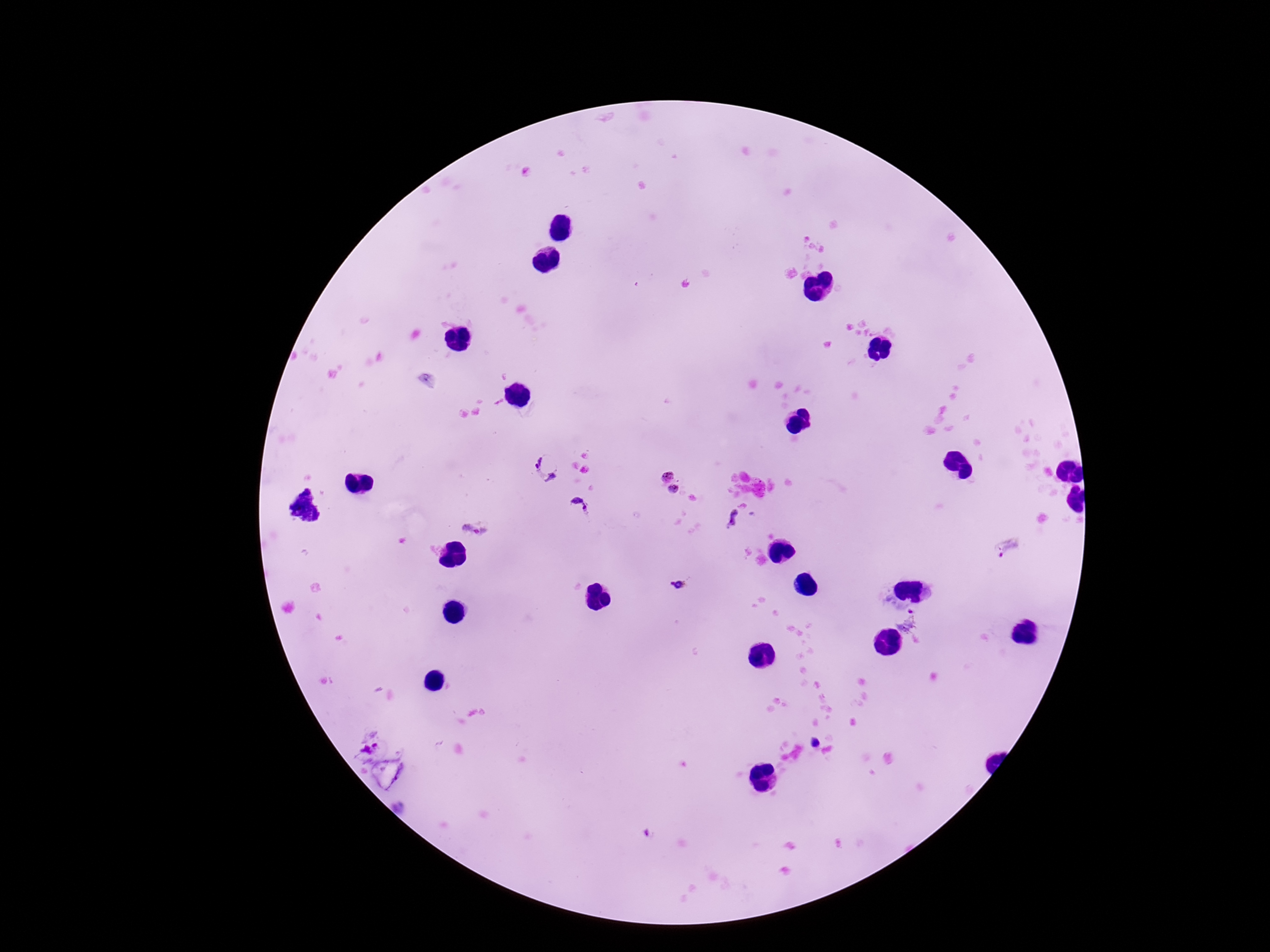

Approximate centers as (x, y) in pixels. Plasmodium parasite locations: (550, 467), (667, 475), (676, 490), (577, 509), (733, 518), (475, 529), (1008, 547), (677, 585), (908, 622), (370, 751). Thick blood film. Patient malaria status: positive. Giemsa-stained preparation. One field from this slide. Image is 1270×952 pixels. 100x magnification. Photographed through the microscope eyepiece with a smartphone camera.